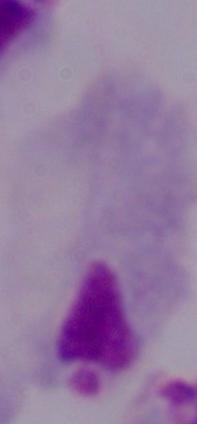

Summary:
  - Modality: photomicrograph
  - Identification: trichomonad
  - Magnification: 1000x